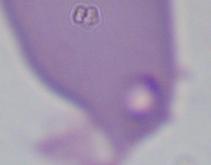
Photomicrograph. Captured at 1000x magnification. A Babesia parasite is seen.